State the preparation type.
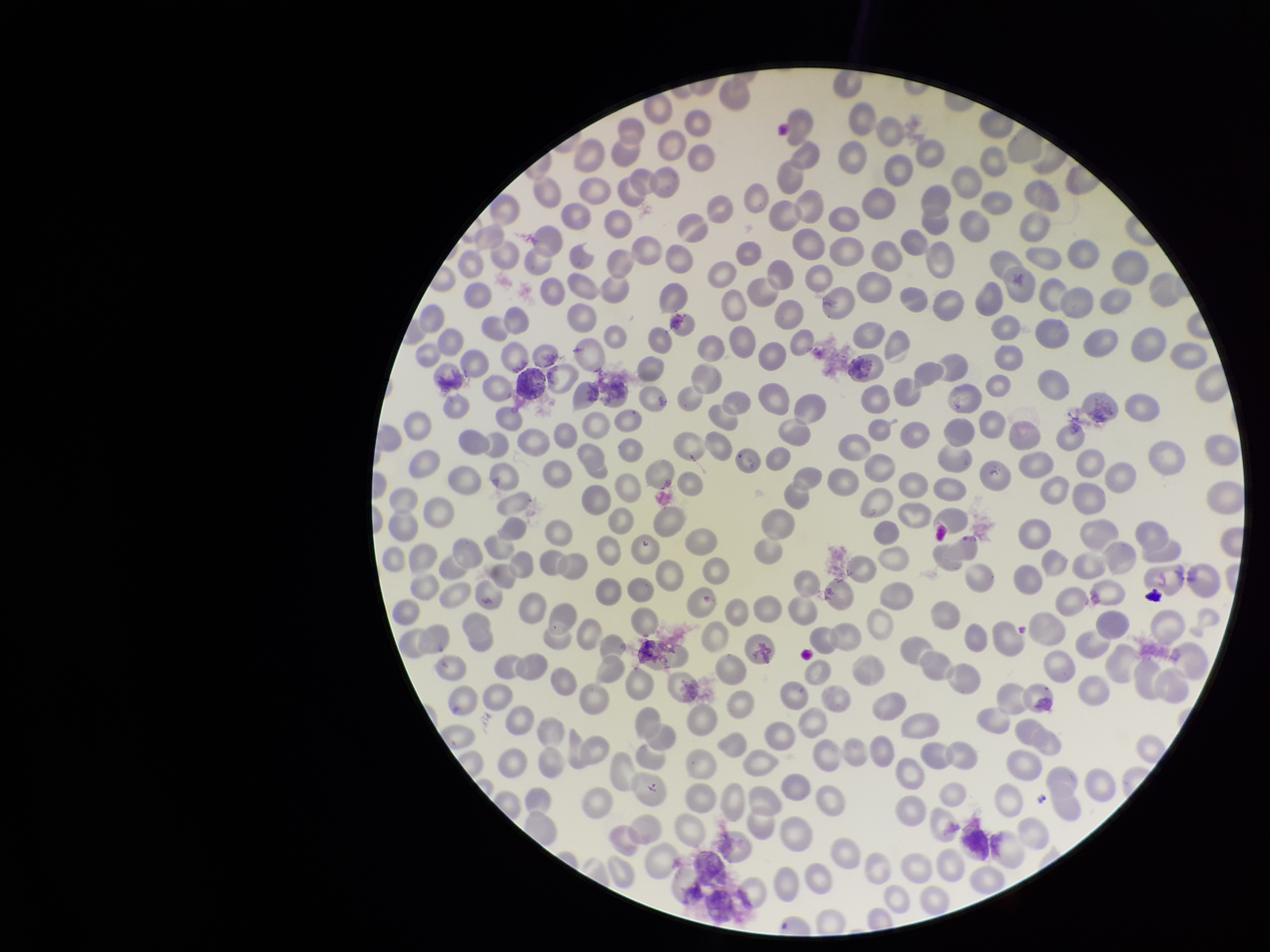

A thin smear.

Summary:
  - Parasitized red blood cells: none seen
  - Red blood cell count: 290
  - Patient malaria status: negative
  - Stain: Giemsa
  - Field of view: single
  - Parasitized red blood cell count: 0
  - Capture: smartphone photograph through the microscope eyepiece
  - Image size: 1270×952 pixels